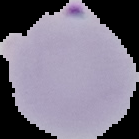
{
  "preparation": "thin blood smear",
  "image_size": "139×139 pixels",
  "image_type": "segmented cell region on a black background",
  "malaria_status": "parasitized"
}